Report the malaria status of this cell.
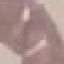

Uninfected.

image type = automatically extracted cell patch, resized to 64 × 64 pixels
preparation = thin smear
stain = Giemsa
capture = smartphone camera at the microscope eyepiece